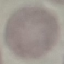

Summary:
  - Result: no malaria parasites detected
  - Image type: cell patch, automatically extracted from a larger field of view and resized to 64 × 64 pixels
  - Capture: smartphone camera at the microscope eyepiece
  - Stain: Giemsa
  - Preparation: thin blood smear